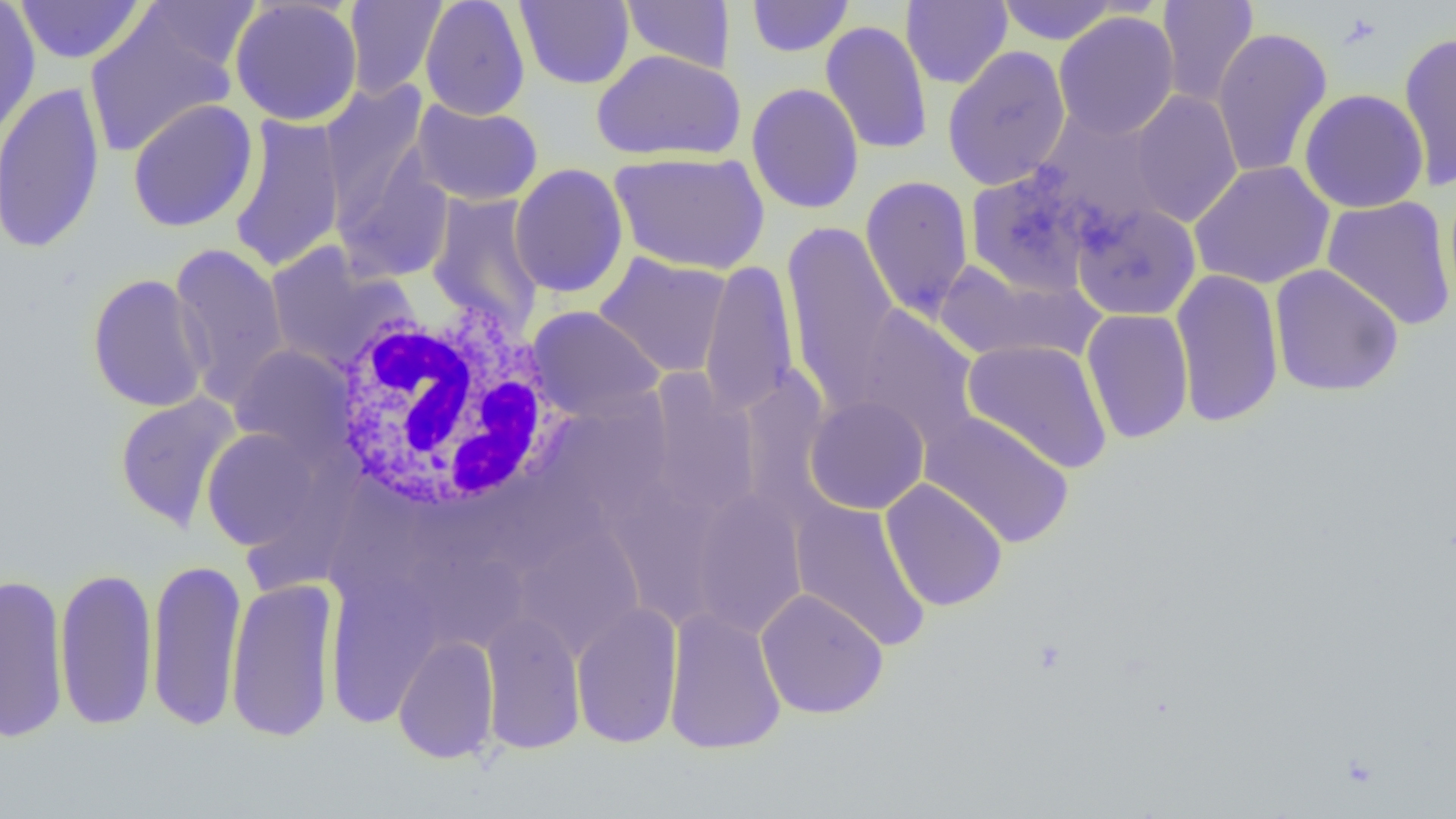
Summary:
  - Coordinate format: approximate bounding boxes as [x1, y1, x2, y2] in pixels
  - White blood cell locations: [321, 293, 568, 517]
  - Uninfected red blood cell locations: [0, 0, 41, 144], [15, 0, 145, 65], [138, 0, 261, 75], [229, 0, 363, 126], [342, 0, 448, 100], [420, 0, 531, 120], [515, 0, 634, 90], [746, 0, 854, 58], [1156, 0, 1259, 107], [621, 1, 736, 74], [901, 1, 1013, 89], [996, 1, 1119, 45], [84, 9, 238, 157], [1053, 12, 1180, 140], [820, 20, 933, 155], [1211, 27, 1333, 179], [1397, 30, 1456, 191], [941, 45, 1071, 191], [592, 49, 745, 163], [0, 80, 106, 255], [746, 82, 865, 214], [319, 84, 431, 228], [1299, 88, 1429, 213], [1129, 90, 1243, 227], [126, 99, 259, 233], [411, 100, 544, 206], [1033, 110, 1171, 232], [228, 113, 347, 274], [332, 150, 454, 284], [609, 151, 769, 275], [1189, 161, 1335, 290], [509, 163, 629, 298], [966, 167, 1097, 296], [860, 175, 974, 320], [426, 192, 545, 335], [1321, 196, 1455, 331], [1069, 201, 1201, 321], [781, 220, 902, 407], [170, 243, 289, 405], [265, 245, 406, 373], [594, 252, 733, 378], [932, 258, 1100, 365], [698, 259, 800, 417], [1268, 264, 1404, 397], [1170, 269, 1285, 428], [86, 273, 212, 412], [846, 304, 982, 450], [527, 306, 665, 420], [1081, 308, 1194, 444], [961, 338, 1113, 473], [229, 344, 356, 462], [739, 365, 834, 526], [647, 370, 761, 520], [114, 392, 241, 531], [804, 395, 930, 515], [919, 410, 1074, 549], [201, 428, 323, 550], [608, 476, 718, 623], [323, 477, 419, 609], [880, 478, 1008, 611], [485, 480, 609, 573], [690, 489, 808, 640], [789, 500, 932, 651], [516, 525, 645, 657], [410, 548, 530, 655], [146, 556, 246, 732], [54, 566, 159, 732], [0, 572, 70, 744], [326, 575, 441, 727], [225, 576, 340, 743], [756, 587, 889, 719], [571, 601, 683, 749], [663, 607, 786, 754], [480, 610, 586, 754], [392, 634, 500, 764]
  - Slide-level diagnosis: no evidence of blood parasites
  - Modality: optical microscopy
  - Field of view: one of a larger specimen
  - Image size: 1456×819 pixels
  - Preparation: thin blood film
  - Magnification: 1000x